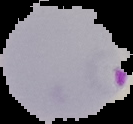
image_size: 133×124 pixels
malaria_status: parasitized
preparation: thin blood film
image_type: segmented cell region on a black background